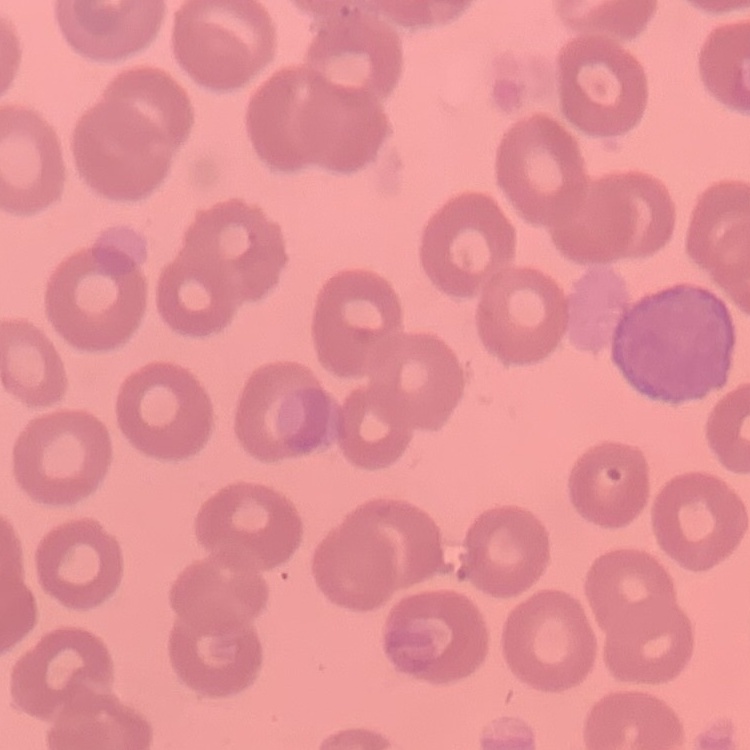
Summary:
  - Red blood cell morphology: no rouleaux formation
  - Stain: Field's or Giemsa
  - Preparation: thin peripheral smear
  - Image type: square crop of a larger photomicrograph